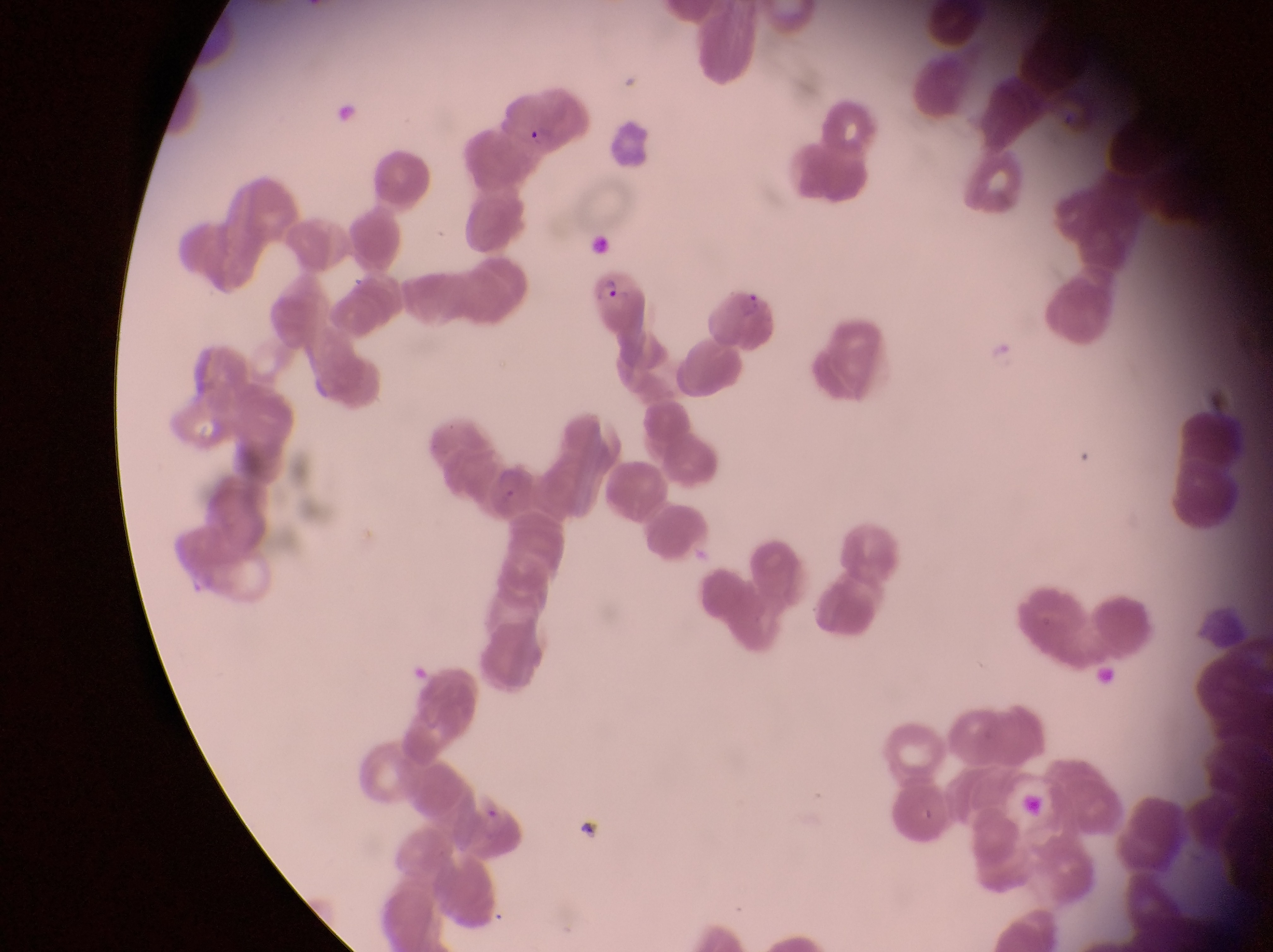
field of view = single
country = Uganda
trophozoite locations = approximate bounding boxes as {left, top, right, bottom} in pixels: {521, 120, 554, 150}, {594, 274, 622, 307}
capture = smartphone photograph through the eyepiece of an Olympus CX-23 microscope
image size = 1273×952 pixels
preparation = thin blood film
magnification = 1000x